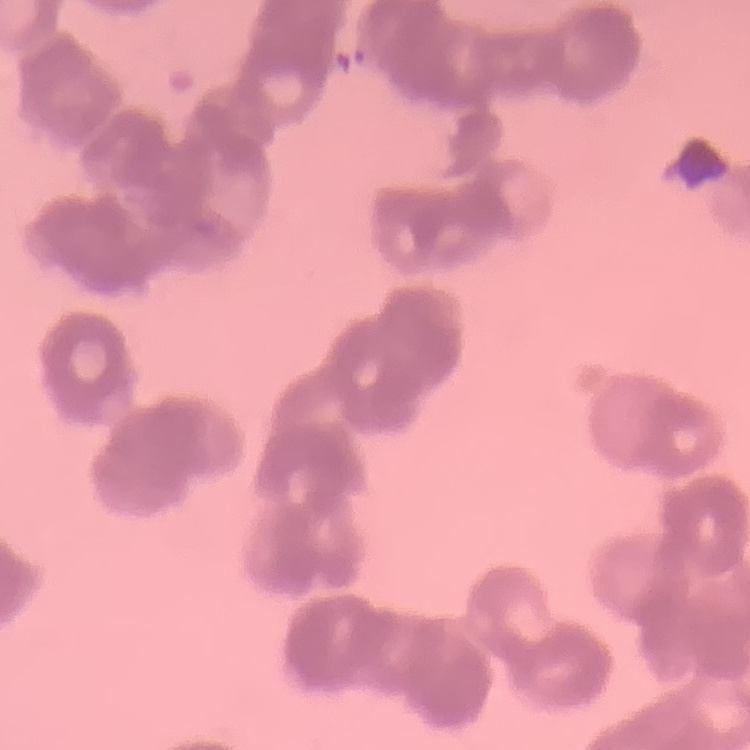

erythrocyte morphology = rouleaux formation
stain = Field's or Giemsa
image type = one tile cut from a larger photomicrograph
preparation = thin peripheral smear